Outline each Plasmodium vivax-infected red blood cell.
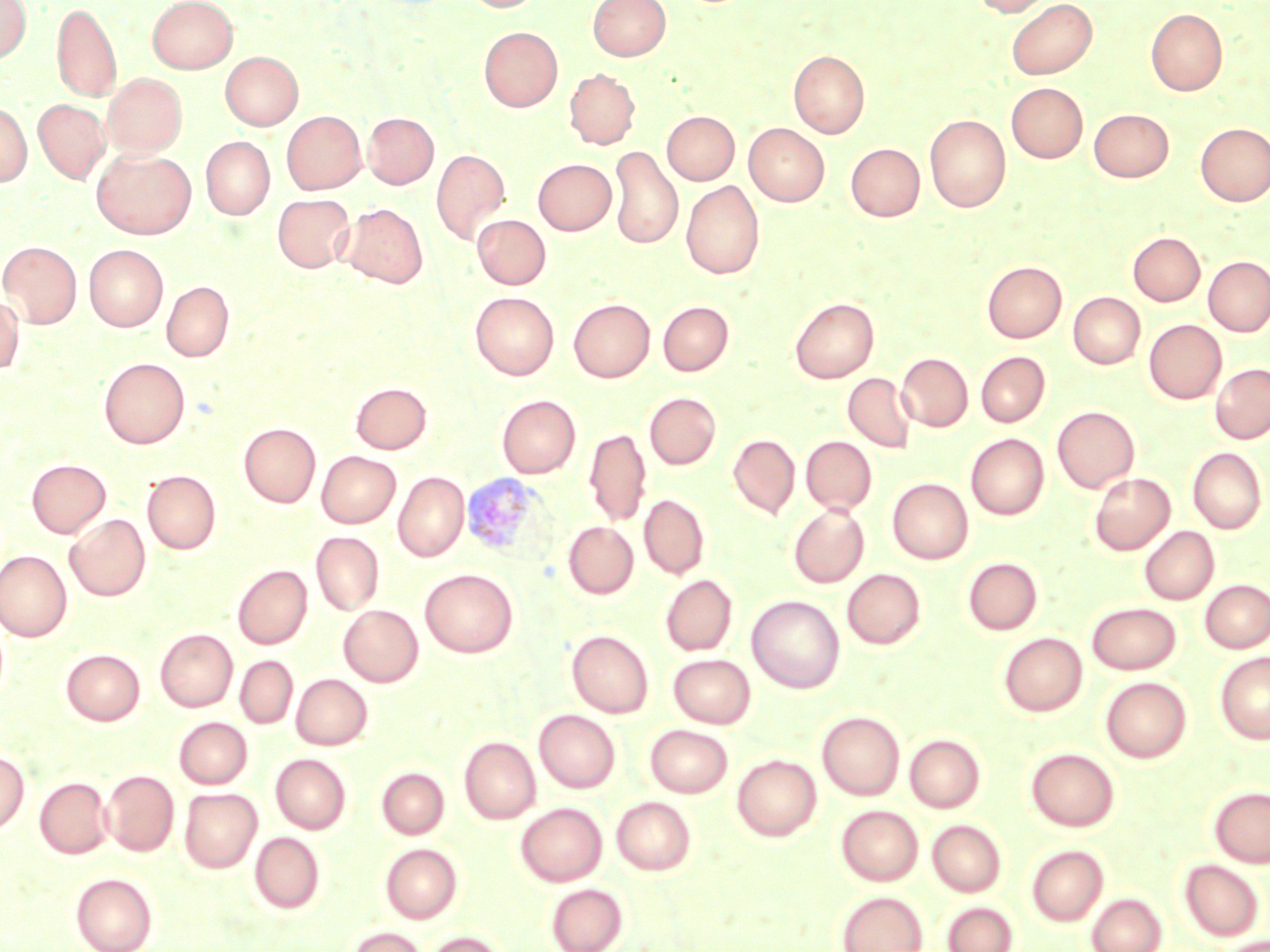
Approximate bounding boxes as named x1/y1/x2/y2 corners in pixels.
Plasmodium vivax-infected red blood cells: (x1=470, y1=474, x2=559, y2=566).

Summary:
  - Uninfected red blood cell locations: (x1=0, y1=0, x2=32, y2=63), (x1=148, y1=0, x2=237, y2=73), (x1=463, y1=0, x2=543, y2=13), (x1=588, y1=0, x2=670, y2=60), (x1=972, y1=0, x2=1053, y2=17), (x1=1006, y1=0, x2=1097, y2=80), (x1=52, y1=3, x2=121, y2=101), (x1=1146, y1=8, x2=1227, y2=96), (x1=479, y1=27, x2=562, y2=111), (x1=789, y1=50, x2=869, y2=138), (x1=220, y1=51, x2=303, y2=130), (x1=564, y1=69, x2=639, y2=149), (x1=103, y1=73, x2=187, y2=157), (x1=1007, y1=83, x2=1088, y2=163), (x1=34, y1=99, x2=110, y2=183), (x1=0, y1=102, x2=32, y2=186), (x1=1089, y1=109, x2=1174, y2=181), (x1=282, y1=111, x2=366, y2=194), (x1=663, y1=111, x2=739, y2=184), (x1=363, y1=112, x2=439, y2=188), (x1=925, y1=114, x2=1011, y2=212), (x1=744, y1=123, x2=829, y2=206), (x1=1196, y1=123, x2=1270, y2=206), (x1=200, y1=137, x2=274, y2=219), (x1=847, y1=139, x2=1010, y2=218), (x1=846, y1=143, x2=924, y2=221), (x1=609, y1=146, x2=682, y2=250), (x1=431, y1=148, x2=510, y2=244), (x1=92, y1=149, x2=196, y2=239), (x1=533, y1=159, x2=616, y2=234), (x1=681, y1=180, x2=764, y2=279), (x1=273, y1=194, x2=355, y2=273), (x1=340, y1=203, x2=428, y2=288), (x1=473, y1=214, x2=551, y2=289), (x1=1129, y1=232, x2=1205, y2=306), (x1=1, y1=241, x2=81, y2=327), (x1=84, y1=245, x2=168, y2=330), (x1=1203, y1=256, x2=1270, y2=336), (x1=982, y1=261, x2=1066, y2=342), (x1=162, y1=280, x2=233, y2=361), (x1=470, y1=292, x2=559, y2=379), (x1=1068, y1=292, x2=1145, y2=368), (x1=0, y1=293, x2=23, y2=375), (x1=790, y1=297, x2=879, y2=382), (x1=568, y1=298, x2=655, y2=382), (x1=658, y1=301, x2=733, y2=375), (x1=1144, y1=319, x2=1226, y2=403), (x1=976, y1=352, x2=1050, y2=426), (x1=896, y1=353, x2=973, y2=431), (x1=99, y1=357, x2=189, y2=447), (x1=1210, y1=363, x2=1270, y2=443), (x1=843, y1=372, x2=917, y2=452), (x1=351, y1=382, x2=431, y2=454), (x1=644, y1=392, x2=721, y2=469), (x1=497, y1=395, x2=580, y2=478), (x1=1052, y1=406, x2=1139, y2=492), (x1=240, y1=422, x2=321, y2=507), (x1=584, y1=427, x2=651, y2=526), (x1=966, y1=433, x2=1049, y2=520), (x1=728, y1=434, x2=800, y2=518), (x1=801, y1=436, x2=876, y2=513), (x1=1188, y1=447, x2=1267, y2=533), (x1=316, y1=451, x2=401, y2=527), (x1=27, y1=459, x2=110, y2=537), (x1=142, y1=470, x2=221, y2=554), (x1=393, y1=471, x2=469, y2=561), (x1=1089, y1=473, x2=1175, y2=554), (x1=887, y1=477, x2=973, y2=564), (x1=639, y1=493, x2=710, y2=579), (x1=788, y1=504, x2=869, y2=587), (x1=65, y1=514, x2=150, y2=601), (x1=564, y1=521, x2=638, y2=599), (x1=1139, y1=526, x2=1219, y2=604), (x1=311, y1=532, x2=384, y2=616), (x1=0, y1=549, x2=72, y2=642), (x1=963, y1=557, x2=1042, y2=635), (x1=233, y1=565, x2=312, y2=649), (x1=420, y1=568, x2=518, y2=657), (x1=842, y1=569, x2=925, y2=649), (x1=660, y1=575, x2=737, y2=655), (x1=1200, y1=579, x2=1270, y2=653), (x1=747, y1=595, x2=845, y2=693), (x1=1087, y1=602, x2=1181, y2=674), (x1=339, y1=605, x2=423, y2=686), (x1=155, y1=628, x2=237, y2=712), (x1=567, y1=630, x2=653, y2=717), (x1=998, y1=633, x2=1087, y2=716), (x1=61, y1=649, x2=145, y2=725), (x1=1215, y1=651, x2=1270, y2=744), (x1=668, y1=654, x2=756, y2=728), (x1=235, y1=655, x2=298, y2=728), (x1=291, y1=674, x2=372, y2=750), (x1=1101, y1=676, x2=1191, y2=762), (x1=534, y1=709, x2=620, y2=793), (x1=817, y1=711, x2=905, y2=800), (x1=174, y1=717, x2=252, y2=788), (x1=645, y1=724, x2=732, y2=797), (x1=905, y1=734, x2=986, y2=812), (x1=459, y1=736, x2=540, y2=823), (x1=1026, y1=747, x2=1119, y2=832), (x1=0, y1=750, x2=29, y2=834), (x1=271, y1=754, x2=351, y2=834), (x1=732, y1=754, x2=821, y2=841), (x1=377, y1=767, x2=449, y2=839), (x1=102, y1=769, x2=179, y2=856), (x1=35, y1=777, x2=113, y2=858), (x1=1209, y1=786, x2=1270, y2=867), (x1=179, y1=788, x2=262, y2=872), (x1=612, y1=797, x2=695, y2=874), (x1=516, y1=803, x2=607, y2=886), (x1=836, y1=805, x2=923, y2=886), (x1=927, y1=819, x2=1006, y2=897), (x1=250, y1=832, x2=325, y2=913), (x1=381, y1=843, x2=462, y2=922), (x1=1026, y1=845, x2=1108, y2=926), (x1=1179, y1=860, x2=1264, y2=941), (x1=71, y1=872, x2=157, y2=952), (x1=546, y1=883, x2=628, y2=952), (x1=836, y1=891, x2=928, y2=952), (x1=1087, y1=893, x2=1166, y2=952), (x1=943, y1=901, x2=1018, y2=952), (x1=346, y1=927, x2=427, y2=952), (x1=423, y1=931, x2=508, y2=952), (x1=1219, y1=935, x2=1269, y2=952)
  - Slide-level diagnosis: Plasmodium vivax
  - Magnification: 1000x
  - Image size: 1270×952 pixels
  - Modality: optical microscopy
  - Field of view: single
  - Stain: May-Grünwald-Giemsa
  - Preparation: thin blood film